Name the parasite shown.
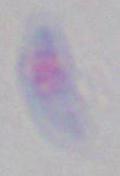
Toxoplasma gondii.

Captured at 1000x magnification. Micrograph.